Assess this cell for malaria.
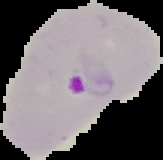
Parasitized.

image type = cell region segmented out of the field of view; surrounding area masked to black
image size = 163×160 pixels
preparation = thin blood film